Report the malaria status of this cell.
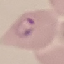
It is parasitized.

Summary:
  - Stain: Giemsa
  - Capture: smartphone camera at the microscope eyepiece
  - Preparation: thin blood film
  - Image type: automatically extracted cell patch, resized to 64 × 64 pixels